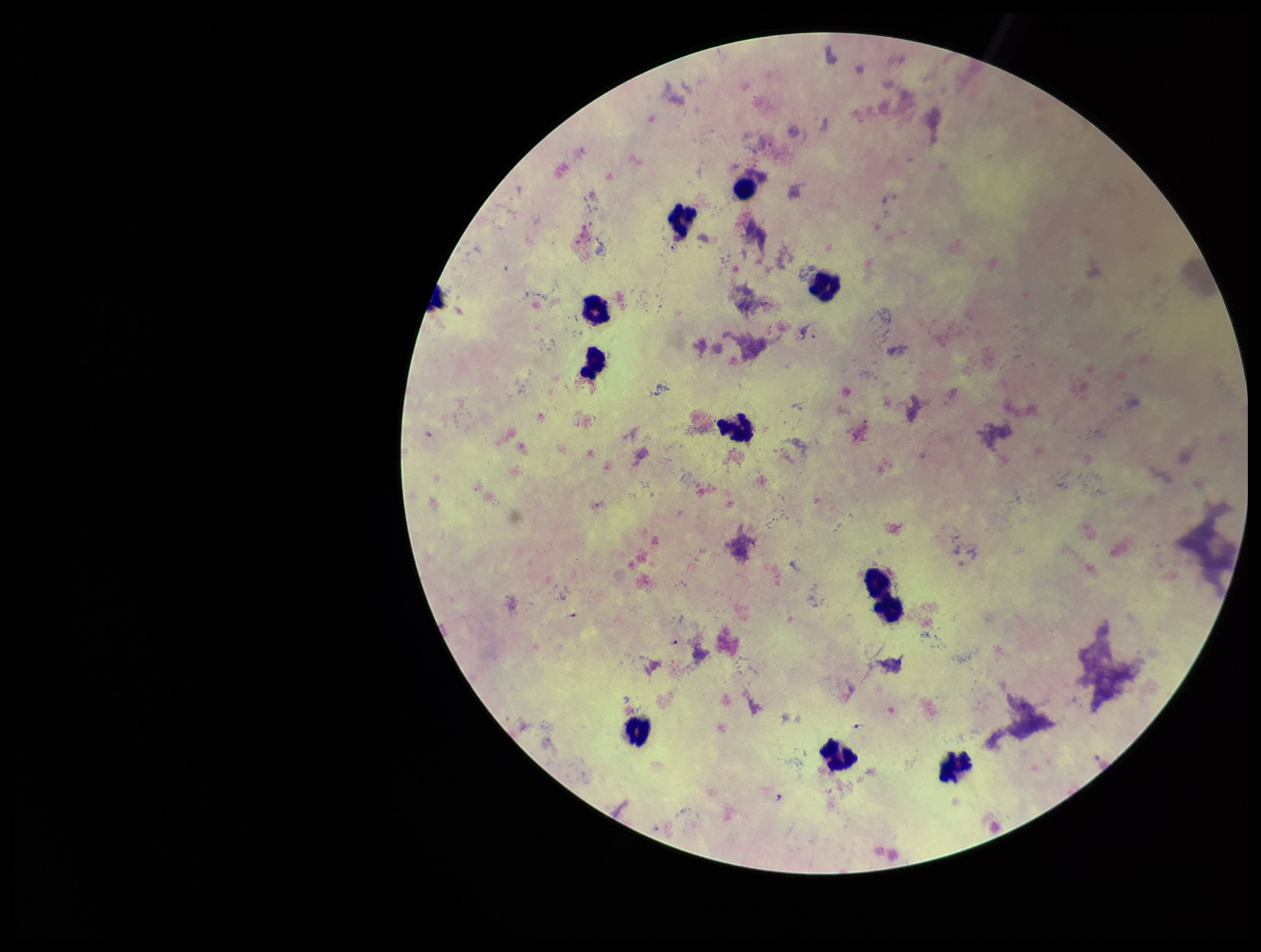

Parasite count: 3. Photographed through the microscope eyepiece with a smartphone camera. Preparation: thick blood smear. Plasmodium parasites: detected. Patient malaria status: positive. Species reported for this patient: Plasmodium falciparum. One field from this slide. Leukocyte count: 10. Giemsa stain. Image is 1261×952 pixels.